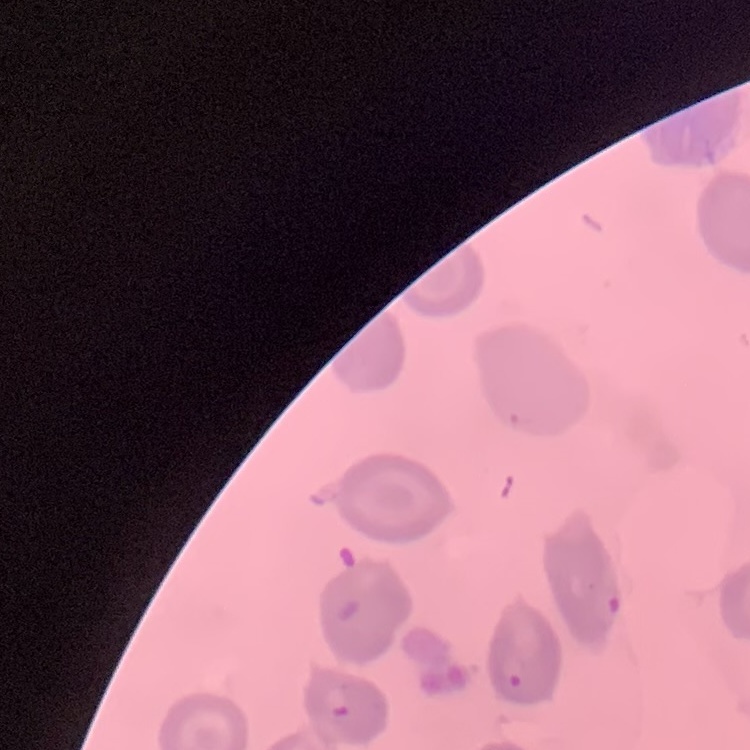 The erythrocytes show no rouleaux formation. Thin peripheral smear. One tile cut from a larger photomicrograph. Stained with either Field's or Giemsa.